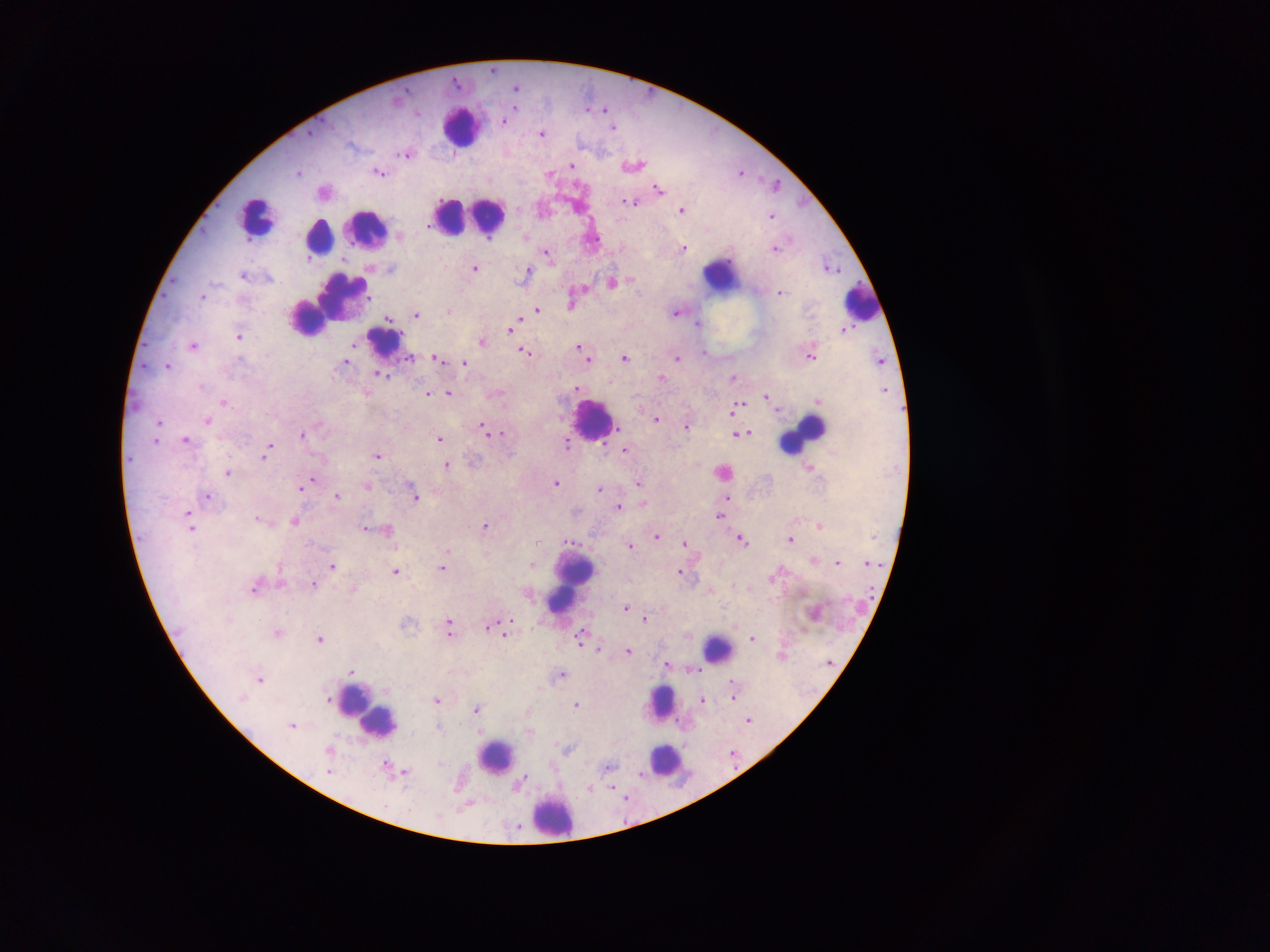

field_of_view: single
capture: mobile-phone photograph through a microscope
plasmodium_parasite_locations: 'approximate centers as [x, y] in pixels: [517, 89], [504, 122], [615, 130], [541, 135], [407, 155], [572, 167], [635, 167], [380, 173], [741, 174], [550, 175], [658, 191], [324, 193], [630, 204], [682, 211], [772, 219], [525, 240], [684, 250], [774, 250], [546, 255], [475, 270], [528, 273], [244, 276], [612, 285], [781, 295], [572, 306], [537, 312], [450, 313], [677, 315], [415, 317], [389, 319], [698, 326], [511, 328], [239, 337], [483, 345], [194, 348], [578, 348], [525, 354], [810, 357], [438, 360], [587, 360], [624, 361], [677, 361], [345, 364], [465, 364], [168, 368], [383, 377], [734, 379], [662, 380], [576, 390], [367, 394], [499, 394], [427, 395], [450, 395], [767, 400], [818, 402], [224, 404], [738, 407], [656, 420], [208, 423], [320, 427], [687, 428], [483, 429], [503, 433], [489, 434], [736, 435], [744, 435], [303, 437], [439, 441], [186, 443], [566, 445], [624, 450], [265, 455], [378, 458], [447, 465], [809, 470], [228, 474], [725, 474], [313, 482], [640, 484], [556, 485], [299, 488], [368, 488], [600, 490], [207, 498], [337, 498], [414, 498], [727, 499], [644, 504], [619, 509], [720, 518], [258, 522], [296, 522], [820, 527], [191, 528], [486, 528], [365, 529], [386, 531], [657, 538], [874, 538], [791, 541], [571, 542], [742, 542], [536, 543], [686, 545], [631, 548], [449, 551], [814, 560], [838, 565], [870, 565], [533, 566], [332, 568], [442, 570], [395, 573], [680, 574], [776, 577], [313, 586], [256, 589], [353, 591], [710, 593], [528, 595], [626, 609], [645, 621], [409, 626], [494, 627], [732, 627], [449, 629], [500, 631], [278, 635], [504, 635], [688, 637], [582, 640], [751, 640], [320, 641], [598, 650], [629, 653], [783, 657], [829, 664], [668, 666], [695, 670], [352, 672], [561, 676], [259, 682], [734, 698], [242, 700], [702, 702], [327, 703], [438, 703], [577, 707], [477, 712], [748, 721], [292, 728], [439, 728], [530, 733], [330, 751], [568, 751], [733, 757], [442, 766], [609, 768], [398, 772], [329, 773], [520, 784], [591, 791], [468, 805], [517, 830]'
leukocyte_locations: 'approximate centers as [x, y] in pixels: [461, 127], [469, 218], [256, 220], [366, 231], [319, 239], [722, 276], [860, 304], [330, 305], [308, 320], [384, 343], [594, 421], [803, 435], [574, 579], [718, 652], [661, 706], [367, 712], [379, 725], [495, 759], [664, 763], [553, 818]'
country: Ghana
image_size: 1270×952 pixels
preparation: thick blood film